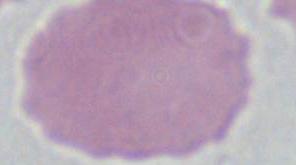
magnification = 1000x
identification = erythrocyte
modality = micrograph